Find the red blood cells and label each as Plasmodium falciparum-infected, uninfected, or of indeterminate infection status.
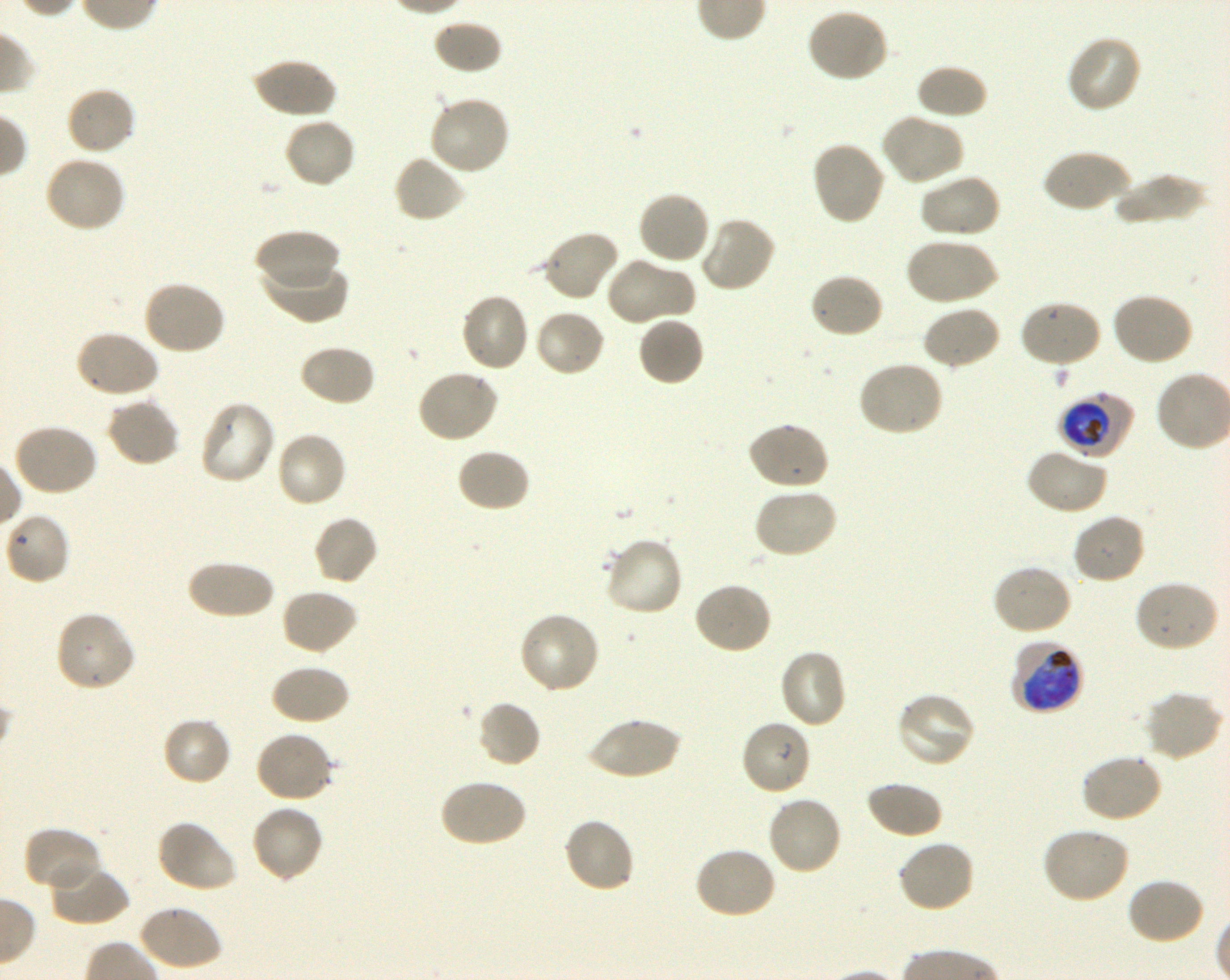
Approximate bounding boxes as [x1, y1, x2, y2] in pixels. Not every red blood cell is marked. A life-cycle stage — or a range of stages, where the recorded stages span more than one — follows each staged infected red blood cell.
Infected red blood cells: [1056, 393, 1133, 458] early trophozoite to early schizont; [1013, 639, 1082, 715] late trophozoite to early schizont.
Uninfected red blood cells: [806, 7, 889, 83], [432, 19, 501, 75], [1066, 34, 1142, 114], [252, 57, 337, 119], [915, 64, 989, 121], [65, 86, 137, 156], [427, 94, 512, 176], [880, 113, 965, 187], [283, 116, 356, 189], [810, 140, 887, 226], [1041, 148, 1132, 214], [392, 153, 467, 224], [43, 154, 126, 234], [918, 173, 1001, 240], [1111, 173, 1208, 225], [637, 191, 711, 266], [698, 216, 777, 294], [255, 228, 339, 291], [538, 229, 621, 302], [905, 236, 999, 307], [261, 255, 348, 324], [605, 256, 695, 326], [808, 272, 885, 340], [141, 279, 226, 356], [1110, 291, 1195, 367], [460, 292, 531, 373], [1019, 299, 1104, 369], [922, 305, 1002, 371], [533, 309, 607, 378], [638, 315, 706, 387], [74, 329, 161, 401], [298, 343, 376, 408], [856, 359, 945, 437], [416, 368, 499, 443], [105, 397, 181, 469], [199, 399, 276, 485], [747, 422, 830, 491], [11, 423, 98, 497], [275, 430, 347, 509], [1025, 447, 1108, 515], [456, 448, 531, 512], [753, 486, 838, 560], [3, 512, 70, 587], [1071, 512, 1147, 586], [312, 515, 379, 586], [602, 535, 683, 618], [186, 559, 274, 620], [991, 563, 1073, 637], [1133, 579, 1220, 653], [692, 581, 772, 656], [279, 587, 358, 655], [54, 610, 137, 692], [518, 610, 602, 695], [778, 649, 847, 730], [269, 664, 350, 725], [1143, 690, 1224, 763], [895, 691, 976, 769], [476, 701, 541, 768], [161, 716, 232, 786], [586, 716, 681, 781], [740, 719, 813, 796], [254, 731, 335, 804], [1080, 754, 1163, 824], [439, 778, 527, 849], [865, 781, 943, 839], [766, 794, 843, 876], [250, 804, 325, 884], [563, 817, 636, 895], [156, 820, 237, 893], [1040, 826, 1131, 904], [23, 827, 102, 894], [897, 839, 976, 914], [694, 846, 778, 921], [46, 861, 128, 927], [1125, 877, 1205, 946], [138, 904, 223, 972].
No red blood cells of indeterminate infection status observed.

Donor blood group O+. Giemsa-stained preparation. Single field of view. Thin blood smear. Image is 1230×980 pixels. 100x objective under oil immersion, numerical aperture 1.30. Plasmodium falciparum strain 3D7 in shaking in-vitro culture.